Identify the parasite.
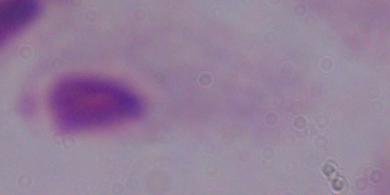
A trichomonad.

Captured at 1000x magnification. Photomicrograph.